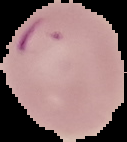
Cell region segmented out of the field of view; the surrounding area is masked to black. From a thin blood smear. Malaria status: parasitized. Image is 127×142 pixels.